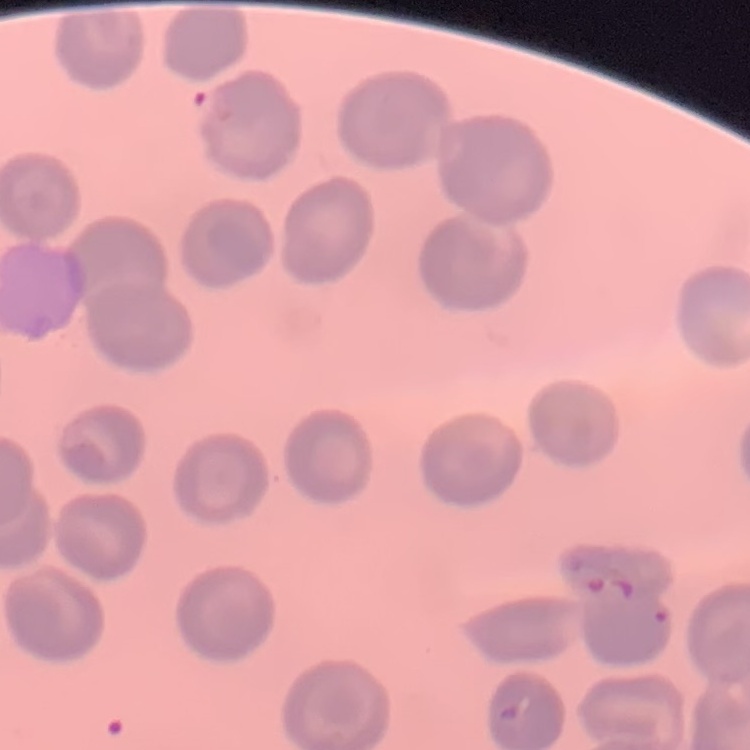
red blood cell morphology = no rouleaux formation
preparation = thin blood film
image type = square crop of a larger photomicrograph
stain = Field's or Giemsa